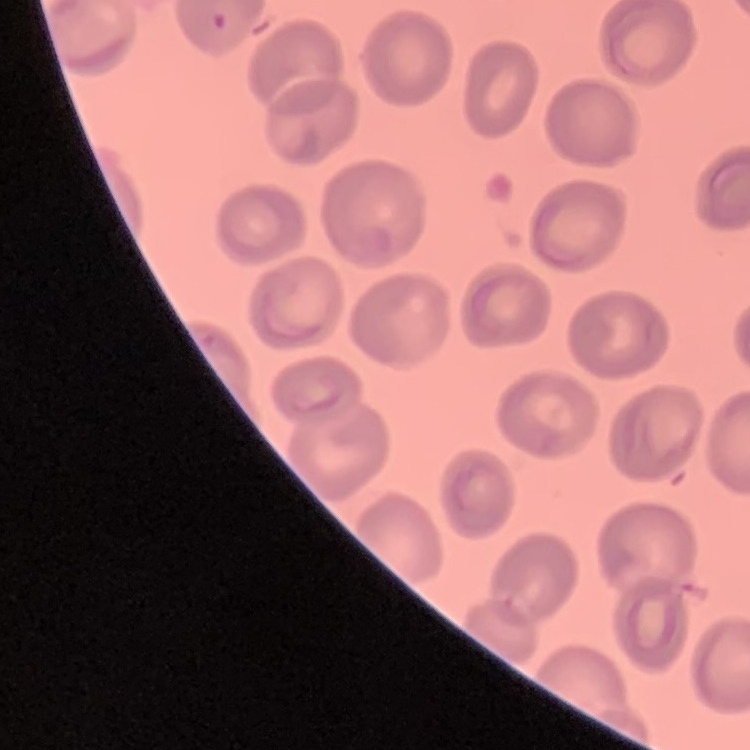 The red blood cells exhibit no rouleaux formation. Thin blood film. Field's or Giemsa stain. Square crop of a larger photomicrograph.